Classify this cell by malaria status.
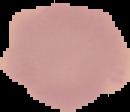
It is uninfected.

Summary:
  - Image size: 130×112 pixels
  - Image type: cell region segmented out of the field of view; surrounding area masked to black
  - Preparation: thin blood smear